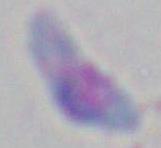
1000x magnification. Toxoplasma gondii is seen. Micrograph.